Assess this cell for malaria.
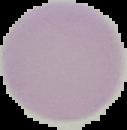

It is uninfected.

Image is 127×130 pixels. From a thin blood film. The area outside the segmented cell region is set to black.